State which parasite is depicted.
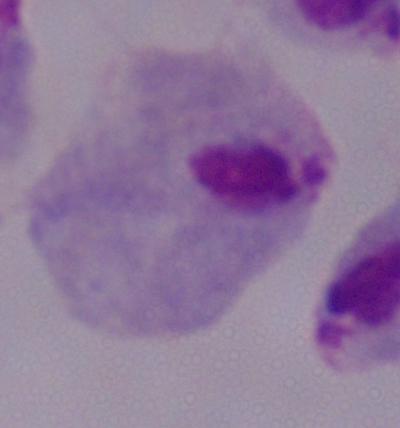

A trichomonad.

Captured at 1000x magnification. Photomicrograph.